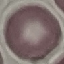

Summary:
  - Result: no malaria parasites seen
  - Capture: smartphone through the microscope eyepiece
  - Preparation: thin blood smear
  - Image type: automatically extracted cell patch, resized to 64 × 64 pixels
  - Stain: Giemsa